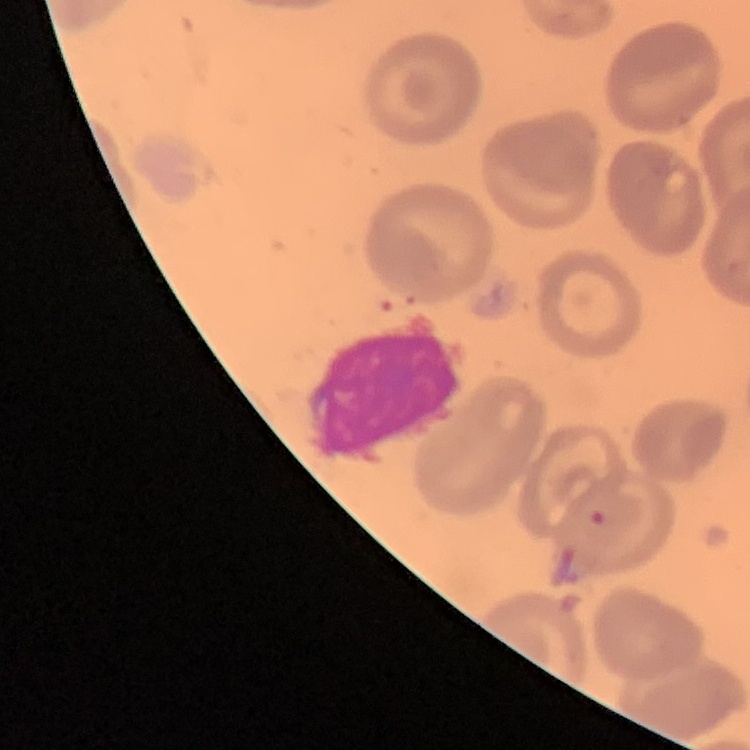

Summary:
  - Red blood cell morphology: no rouleaux formation
  - Preparation: thin blood smear
  - Stain: Field's or Giemsa
  - Image type: one tile cut from a larger photomicrograph